Outline each blood parasite and name the species.
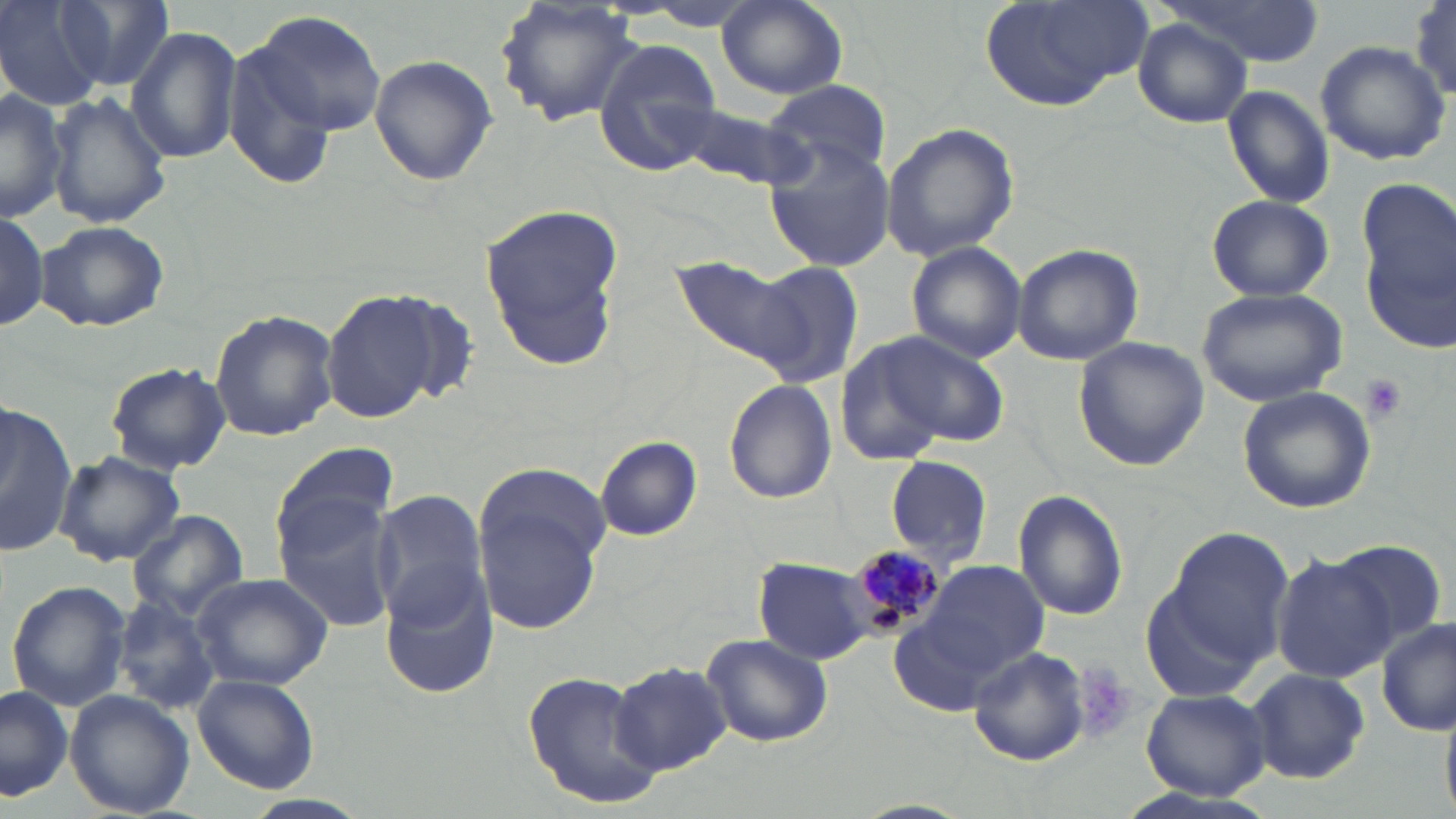

Approximate bounding boxes as [x1, y1, x2, y2] in pixels.
Plasmodium malariae-infected red blood cells: [843, 545, 943, 643].
No Plasmodium falciparum, Plasmodium ovale, Plasmodium vivax, Babesia divergens, or Trypanosoma brucei observed.

Platelet locations: [1361, 373, 1408, 421]. Uninfected red blood cell locations: [0, 0, 107, 110], [59, 0, 177, 91], [977, 0, 1155, 112], [1160, 0, 1326, 65], [1409, 1, 1456, 103], [495, 2, 645, 125], [717, 2, 847, 99], [240, 8, 389, 144], [1133, 19, 1251, 126], [126, 26, 243, 166], [592, 38, 725, 172], [1315, 41, 1452, 166], [369, 53, 498, 186], [764, 79, 892, 182], [1221, 84, 1335, 209], [0, 90, 67, 222], [47, 91, 170, 230], [676, 99, 810, 186], [881, 122, 1021, 261], [764, 137, 899, 272], [1206, 193, 1333, 302], [1358, 200, 1456, 353], [480, 204, 628, 365], [0, 212, 50, 332], [36, 220, 169, 332], [906, 241, 1027, 363], [1012, 243, 1143, 365], [668, 255, 815, 373], [752, 260, 867, 390], [1194, 286, 1348, 408], [322, 288, 445, 423], [384, 292, 481, 407], [209, 309, 340, 441], [856, 330, 1009, 456], [1072, 336, 1210, 471], [105, 361, 231, 475], [722, 380, 838, 505], [1237, 386, 1376, 514], [0, 403, 76, 560], [595, 436, 703, 541], [271, 441, 399, 552], [56, 450, 183, 568], [886, 455, 993, 568], [477, 464, 614, 577], [368, 489, 487, 625], [1013, 490, 1129, 620], [273, 495, 399, 631], [478, 497, 604, 634], [128, 510, 249, 619], [1160, 528, 1298, 676], [1329, 542, 1448, 655], [1271, 551, 1395, 683], [753, 557, 882, 666], [900, 560, 1054, 699], [381, 567, 499, 699], [191, 573, 333, 690], [6, 578, 130, 712], [111, 596, 221, 715], [1377, 617, 1453, 735], [701, 634, 834, 747], [968, 646, 1089, 766], [612, 660, 732, 775], [1246, 667, 1371, 784], [520, 668, 664, 807], [193, 674, 319, 793], [0, 686, 75, 802], [1139, 688, 1273, 802], [66, 690, 194, 817]. Slide-level diagnosis: Plasmodium malariae. Captured at 1000x magnification. Light microscopy. One field of a larger specimen. Image is 1456×819 pixels. Thin blood smear. May-Grünwald-Giemsa-stained preparation.